Point out each Plasmodium parasite.
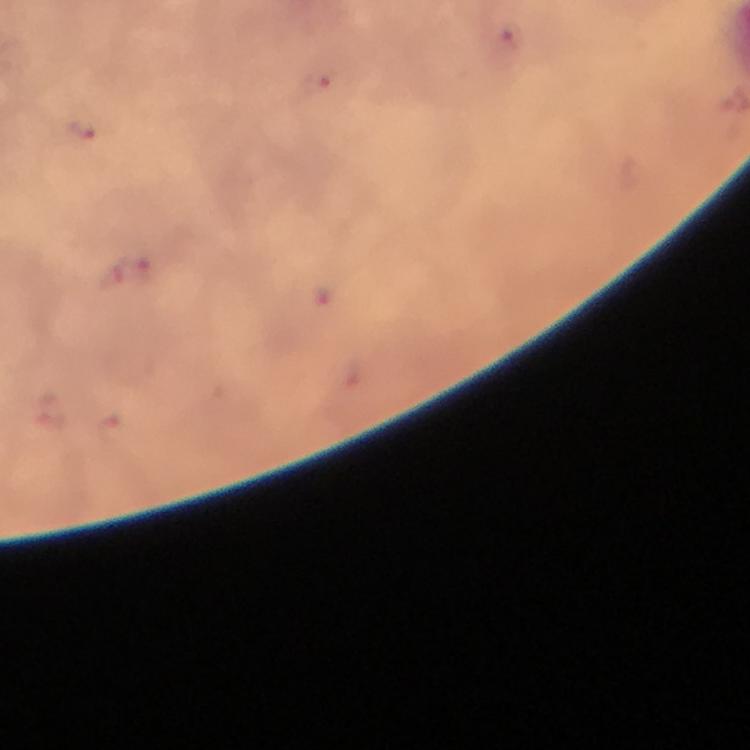
Approximate centers as {x, y} in pixels.
Plasmodium parasites: {511, 38}, {316, 86}, {79, 128}, {144, 272}, {108, 428}.

Summary:
  - Magnification: 100x
  - Image size: 750×750 pixels
  - Cropped from: one field of view
  - Context: from a malaria diagnostic workup
  - Preparation: thick blood smear
  - Stain: Giemsa
  - Immersion oil: applied
  - Capture: smartphone camera through the microscope